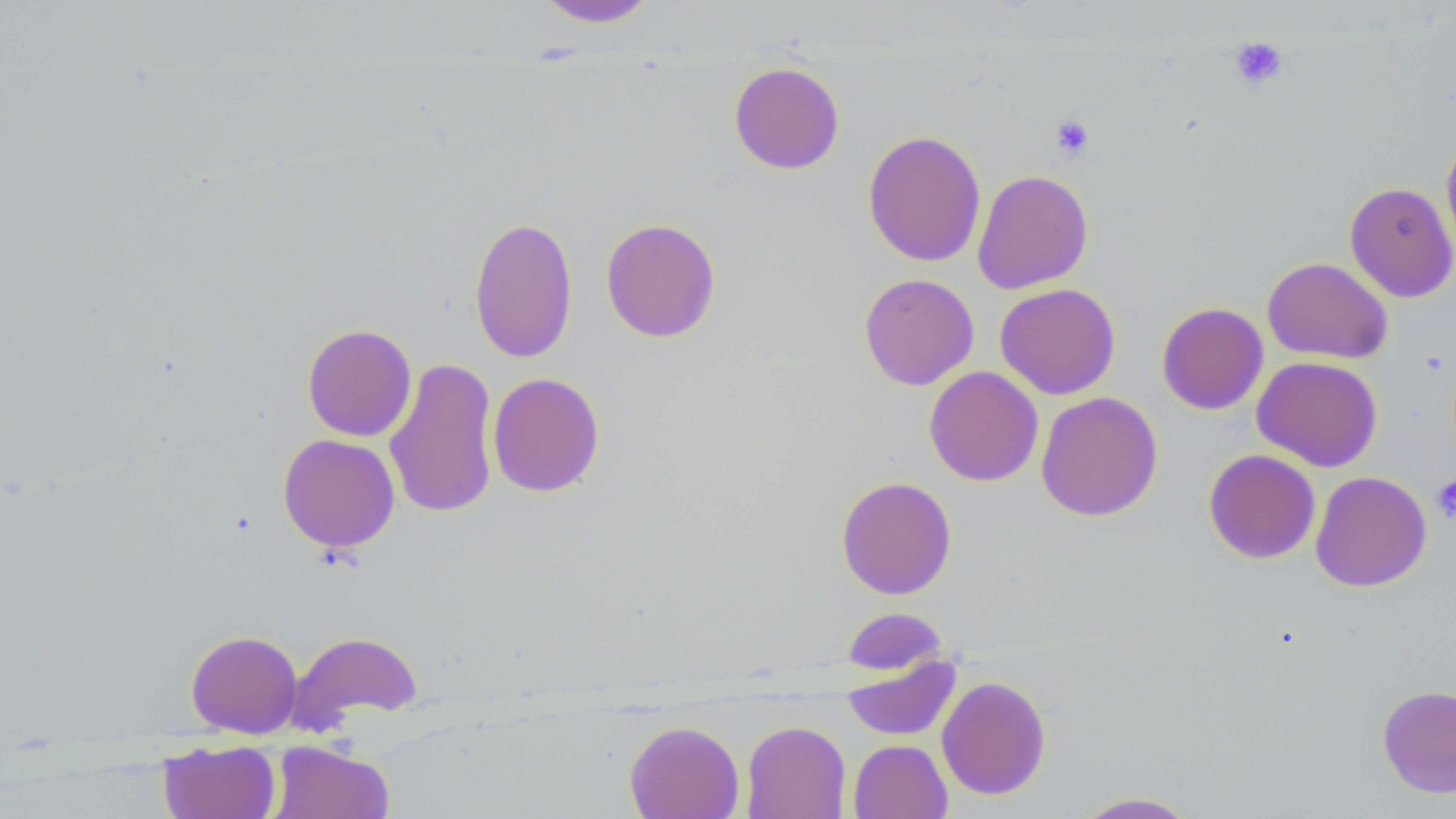

{
  "slide_level_diagnosis": "no evidence of blood parasites",
  "preparation": "thin blood smear",
  "platelet_locations": "approximate bounding boxes as [x1, y1, x2, y2] in pixels: [1228, 36, 1289, 90], [1049, 114, 1095, 160], [1431, 475, 1456, 523]",
  "magnification": "1000x",
  "uninfected_red_blood_cell_locations": "approximate bounding boxes as [x1, y1, x2, y2] in pixels: [533, 0, 661, 28], [728, 63, 845, 175], [862, 129, 986, 267], [1440, 131, 1456, 260], [972, 169, 1093, 294], [1344, 182, 1456, 302], [468, 215, 578, 364], [600, 217, 722, 343], [1262, 257, 1393, 364], [859, 273, 979, 390], [995, 283, 1121, 399], [1156, 302, 1269, 415], [302, 323, 417, 442], [1252, 356, 1383, 472], [384, 358, 500, 519], [924, 366, 1044, 487], [488, 372, 605, 497], [1035, 391, 1163, 522], [277, 433, 400, 553], [1203, 449, 1321, 564], [1310, 470, 1432, 592], [835, 476, 957, 599], [842, 607, 949, 674], [186, 629, 303, 738], [286, 630, 423, 734], [840, 655, 962, 742], [936, 675, 1051, 800], [1377, 684, 1456, 798], [624, 720, 744, 819], [742, 720, 850, 819], [848, 739, 953, 819], [158, 740, 281, 819], [269, 741, 394, 819], [1072, 791, 1201, 818]",
  "stain": "May-Grünwald-Giemsa",
  "field_of_view": "single",
  "modality": "light microscopy",
  "image_size": "1456×819 pixels"
}